Assess this cell for malaria.
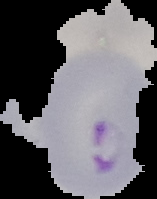
Parasitized.

image type = segmented cell region with the area outside set to black
preparation = thin blood film
image size = 157×199 pixels